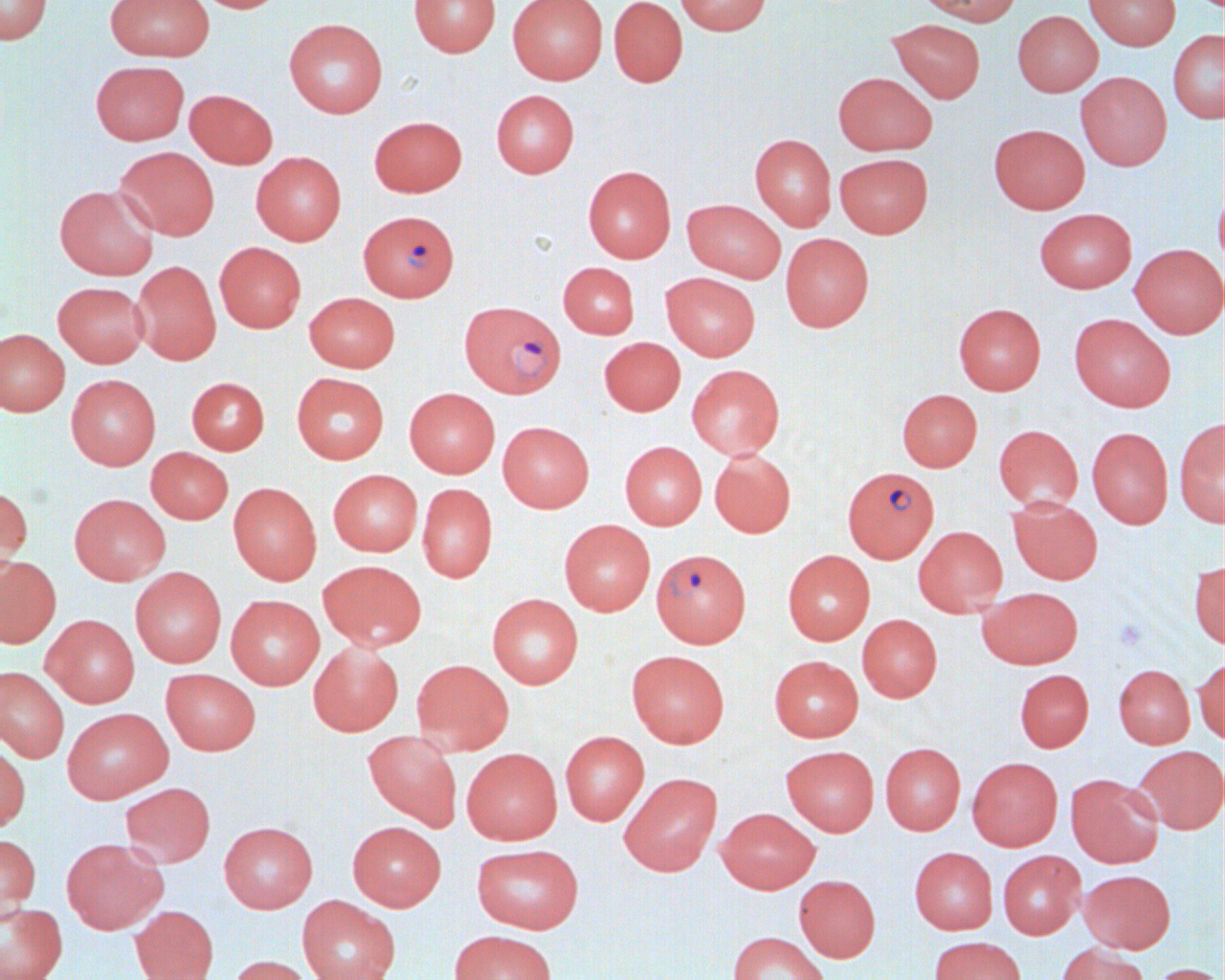

Summary:
  - Coordinate format: approximate bounding boxes as named x1/y1/x2/y2 corners in pixels
  - Plasmodium falciparum-infected red blood cell locations: (x1=358, y1=210, x2=459, y2=301), (x1=459, y1=300, x2=566, y2=399), (x1=842, y1=466, x2=939, y2=562), (x1=651, y1=548, x2=751, y2=647)
  - Uninfected red blood cell locations: (x1=0, y1=0, x2=53, y2=45), (x1=105, y1=0, x2=214, y2=61), (x1=193, y1=0, x2=284, y2=13), (x1=409, y1=0, x2=501, y2=57), (x1=507, y1=0, x2=607, y2=84), (x1=608, y1=0, x2=688, y2=87), (x1=675, y1=0, x2=771, y2=35), (x1=916, y1=0, x2=1023, y2=26), (x1=1083, y1=0, x2=1181, y2=50), (x1=1012, y1=10, x2=1103, y2=96), (x1=284, y1=18, x2=388, y2=118), (x1=888, y1=18, x2=986, y2=102), (x1=1168, y1=30, x2=1224, y2=123), (x1=90, y1=60, x2=189, y2=145), (x1=1076, y1=71, x2=1172, y2=171), (x1=833, y1=72, x2=937, y2=155), (x1=184, y1=89, x2=277, y2=169), (x1=491, y1=89, x2=579, y2=178), (x1=369, y1=116, x2=467, y2=197), (x1=989, y1=123, x2=1090, y2=214), (x1=750, y1=133, x2=836, y2=231), (x1=114, y1=146, x2=220, y2=240), (x1=251, y1=151, x2=346, y2=245), (x1=835, y1=153, x2=933, y2=237), (x1=583, y1=165, x2=676, y2=263), (x1=1214, y1=182, x2=1224, y2=276), (x1=54, y1=184, x2=159, y2=280), (x1=682, y1=199, x2=786, y2=283), (x1=1034, y1=208, x2=1137, y2=293), (x1=780, y1=233, x2=874, y2=332), (x1=214, y1=242, x2=306, y2=332), (x1=1129, y1=243, x2=1224, y2=338), (x1=132, y1=260, x2=221, y2=365), (x1=558, y1=262, x2=639, y2=338), (x1=660, y1=272, x2=760, y2=361), (x1=53, y1=281, x2=149, y2=367), (x1=304, y1=292, x2=399, y2=372), (x1=954, y1=303, x2=1046, y2=395), (x1=1069, y1=313, x2=1175, y2=412), (x1=0, y1=328, x2=69, y2=416), (x1=599, y1=337, x2=686, y2=416), (x1=686, y1=364, x2=785, y2=460), (x1=291, y1=372, x2=389, y2=464), (x1=66, y1=374, x2=161, y2=470), (x1=187, y1=377, x2=269, y2=455), (x1=404, y1=387, x2=500, y2=478), (x1=897, y1=389, x2=982, y2=472), (x1=1174, y1=417, x2=1225, y2=526), (x1=497, y1=421, x2=594, y2=512), (x1=993, y1=424, x2=1083, y2=511), (x1=1087, y1=426, x2=1173, y2=528), (x1=619, y1=441, x2=707, y2=529), (x1=146, y1=447, x2=233, y2=524), (x1=709, y1=449, x2=796, y2=538), (x1=328, y1=469, x2=422, y2=556), (x1=228, y1=482, x2=322, y2=585), (x1=417, y1=483, x2=498, y2=583), (x1=0, y1=484, x2=32, y2=583), (x1=69, y1=493, x2=170, y2=585), (x1=1008, y1=496, x2=1103, y2=585), (x1=559, y1=519, x2=655, y2=616), (x1=913, y1=526, x2=1008, y2=616), (x1=783, y1=550, x2=875, y2=645), (x1=0, y1=556, x2=61, y2=648), (x1=317, y1=559, x2=427, y2=651), (x1=1189, y1=560, x2=1225, y2=650), (x1=130, y1=567, x2=226, y2=667), (x1=978, y1=586, x2=1083, y2=669), (x1=487, y1=593, x2=583, y2=689), (x1=225, y1=594, x2=325, y2=689), (x1=41, y1=614, x2=140, y2=708), (x1=857, y1=614, x2=942, y2=702), (x1=308, y1=642, x2=403, y2=736), (x1=626, y1=650, x2=730, y2=748), (x1=769, y1=655, x2=864, y2=742), (x1=1194, y1=657, x2=1224, y2=744), (x1=411, y1=659, x2=514, y2=755), (x1=1114, y1=664, x2=1195, y2=748), (x1=0, y1=666, x2=69, y2=763), (x1=161, y1=668, x2=261, y2=755), (x1=1015, y1=668, x2=1094, y2=752), (x1=62, y1=707, x2=173, y2=803), (x1=363, y1=729, x2=462, y2=831), (x1=560, y1=731, x2=649, y2=825), (x1=0, y1=741, x2=30, y2=833), (x1=880, y1=742, x2=966, y2=835), (x1=781, y1=745, x2=879, y2=836), (x1=1132, y1=745, x2=1225, y2=834), (x1=461, y1=747, x2=563, y2=845), (x1=967, y1=756, x2=1063, y2=850), (x1=619, y1=772, x2=722, y2=876), (x1=1065, y1=773, x2=1163, y2=868), (x1=120, y1=782, x2=215, y2=867), (x1=715, y1=807, x2=820, y2=893), (x1=219, y1=821, x2=318, y2=913), (x1=347, y1=821, x2=446, y2=911), (x1=0, y1=833, x2=41, y2=918), (x1=60, y1=838, x2=167, y2=934), (x1=471, y1=843, x2=584, y2=934), (x1=909, y1=847, x2=998, y2=934), (x1=998, y1=850, x2=1085, y2=939), (x1=1079, y1=869, x2=1175, y2=953), (x1=794, y1=874, x2=880, y2=962), (x1=297, y1=895, x2=400, y2=980), (x1=0, y1=901, x2=67, y2=980), (x1=129, y1=905, x2=219, y2=980), (x1=449, y1=929, x2=557, y2=980), (x1=727, y1=931, x2=829, y2=980), (x1=929, y1=936, x2=1027, y2=980), (x1=1056, y1=943, x2=1148, y2=980), (x1=227, y1=955, x2=316, y2=980), (x1=1148, y1=963, x2=1222, y2=980)
  - Slide-level diagnosis: Plasmodium falciparum
  - Field of view: one of a larger specimen
  - Image size: 1225×980 pixels
  - Magnification: 1000x
  - Preparation: thin blood smear
  - Modality: light microscopy